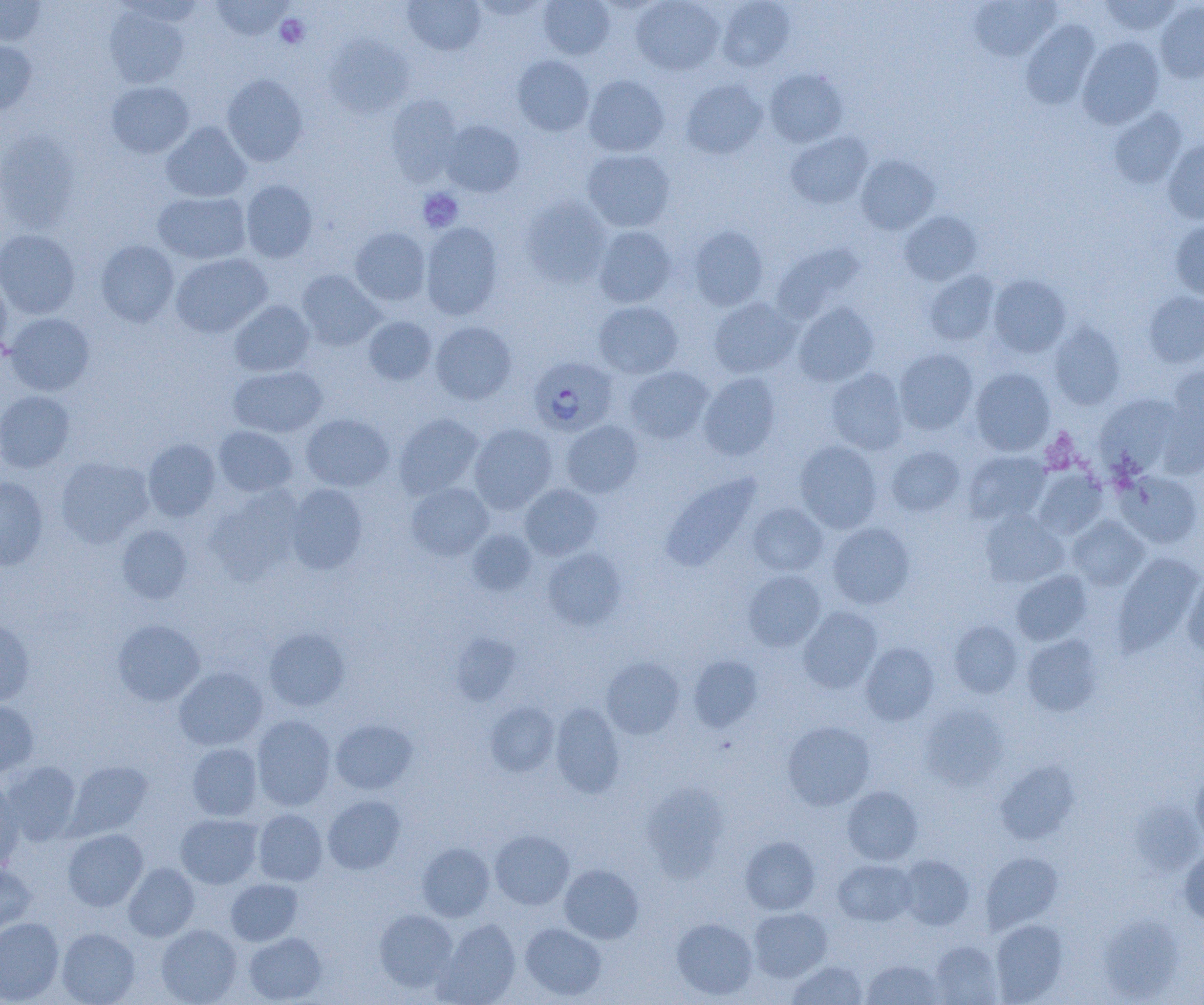 Approximate bounding boxes as (x1,y1)-(x2,y2) corner pairs in pixels. Uninfected red blood cell locations: (210,0)-(293,41), (403,0)-(485,55), (469,0)-(550,19), (537,0)-(615,60), (631,0)-(724,75), (717,0)-(794,72), (1099,0)-(1182,35), (0,1)-(47,46), (968,1)-(1061,61), (1155,2)-(1204,83), (105,7)-(189,88), (1021,20)-(1099,109), (324,36)-(414,119), (1077,36)-(1165,129), (0,41)-(37,116), (512,55)-(594,137), (764,68)-(848,148), (221,73)-(308,166), (583,75)-(669,157), (681,79)-(767,159), (106,81)-(194,157), (385,95)-(462,184), (1108,107)-(1187,188), (441,120)-(524,196), (161,122)-(251,202), (0,131)-(80,233), (785,131)-(873,209), (1162,140)-(1204,224), (582,149)-(675,232), (856,155)-(939,234), (240,180)-(317,262), (153,191)-(250,264), (521,197)-(611,287), (899,211)-(982,286), (1169,219)-(1204,300), (420,222)-(503,320), (593,225)-(677,308), (688,225)-(768,310), (350,227)-(430,306), (0,229)-(80,318), (95,240)-(178,326), (770,242)-(865,324), (170,253)-(272,338), (296,270)-(384,350), (924,270)-(1000,346), (0,273)-(12,361), (988,275)-(1071,358), (1143,291)-(1204,367), (709,297)-(801,378), (229,300)-(314,377), (593,301)-(683,379), (793,302)-(879,386), (5,313)-(95,396), (363,316)-(437,386), (431,321)-(516,404), (1048,321)-(1125,410), (894,348)-(978,434), (1166,364)-(1204,448), (228,365)-(327,438), (623,366)-(713,443), (970,367)-(1055,456), (826,368)-(908,454), (698,373)-(781,460), (0,390)-(75,473), (1095,394)-(1179,477), (394,413)-(483,499), (301,414)-(394,491), (561,420)-(643,498), (469,423)-(557,513), (214,426)-(297,498), (143,439)-(221,521), (795,441)-(882,533), (886,446)-(964,516), (963,450)-(1051,525), (55,456)-(154,548), (1032,467)-(1107,539), (1115,471)-(1202,548), (660,472)-(760,571), (0,476)-(48,570), (406,482)-(494,560), (520,483)-(602,560), (286,484)-(368,574), (206,488)-(303,584), (747,503)-(828,576), (980,510)-(1068,587), (1068,515)-(1149,590), (827,522)-(915,609), (117,525)-(192,604), (467,529)-(536,596), (542,547)-(626,630), (1113,553)-(1202,655), (742,570)-(826,651), (1012,570)-(1092,645), (1182,572)-(1204,659), (799,606)-(882,693), (0,618)-(35,707), (112,619)-(205,706), (949,620)-(1023,698), (264,628)-(350,711), (454,634)-(523,702), (1022,635)-(1103,716), (861,642)-(940,725), (688,655)-(762,732), (602,657)-(684,739), (174,667)-(267,750), (0,701)-(38,777), (485,702)-(559,776), (550,703)-(624,798), (920,704)-(1007,791), (252,715)-(336,811), (330,719)-(417,794), (782,721)-(875,810), (187,743)-(262,820), (3,761)-(82,845), (67,761)-(152,838), (995,761)-(1078,844), (1191,767)-(1204,848), (0,779)-(25,872), (641,783)-(728,880), (842,786)-(923,864), (322,795)-(405,874), (253,809)-(328,886), (176,814)-(262,889), (63,829)-(147,911), (490,830)-(574,910), (740,836)-(820,915), (417,842)-(494,921), (1179,849)-(1204,925), (981,852)-(1062,932), (898,855)-(974,930), (833,859)-(916,926), (0,862)-(36,936), (124,863)-(199,941), (559,864)-(643,944), (226,878)-(302,945), (374,908)-(458,991), (748,908)-(832,981), (1099,914)-(1182,1002), (0,917)-(64,1004), (671,917)-(757,1000), (434,919)-(521,1005), (989,919)-(1067,1003), (520,923)-(606,1001), (156,924)-(242,1005), (57,927)-(140,1005), (244,932)-(326,1004), (930,941)-(1003,1004), (862,959)-(945,1004), (787,961)-(867,1004). Platelet locations: (275,14)-(309,49), (417,188)-(463,232). Plasmodium falciparum-infected red blood cell locations: (529,356)-(618,437). Slide-level diagnosis: Plasmodium falciparum. Light microscopy. Image is 1204×1005 pixels. 1000x magnification. Thin blood film. One field of a larger specimen.